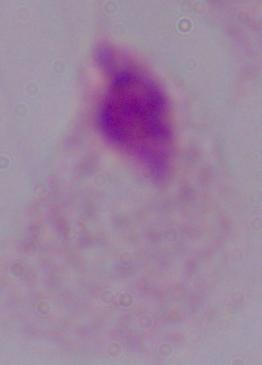

Photomicrograph. Captured at 1000x magnification. A trichomonad is seen.